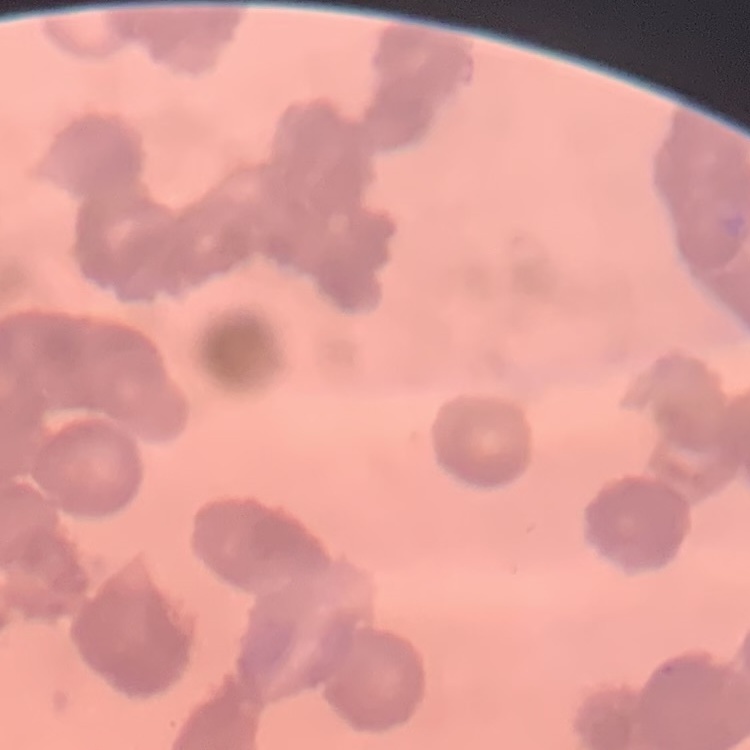
The erythrocytes show rouleaux formation. Thin blood film. One tile cut from a larger photomicrograph. Stained with either Field's or Giemsa.